Assess this cell for malaria.
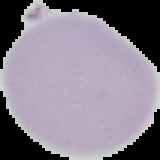
It is uninfected.

image type = cell region segmented out of the field of view; surrounding area masked to black
preparation = thin blood smear
image size = 160×160 pixels